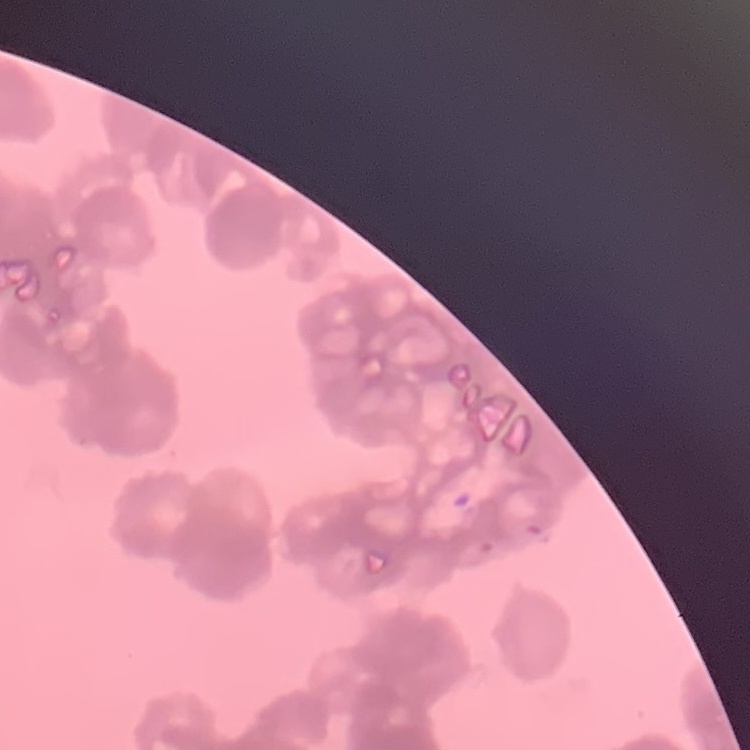 The erythrocytes show rouleaux formation. Thin blood smear. Stained with either Field's or Giemsa. Square crop of a larger photomicrograph.